State which parasite is depicted.
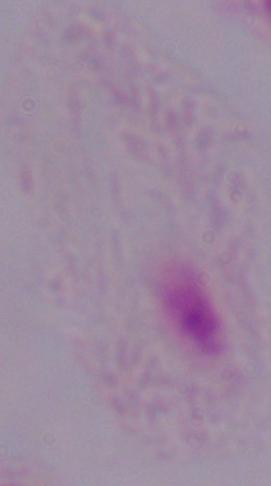

This is a trichomonad.

Summary:
  - Magnification: 1000x
  - Modality: micrograph